Classify this cell by malaria status.
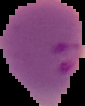

Parasitized.

image size = 85×106 pixels
preparation = thin blood smear
image type = segmented cell region on a black background